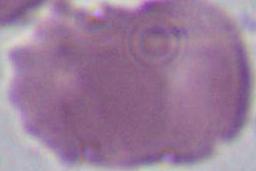
identification = erythrocyte
modality = photomicrograph
magnification = 1000x